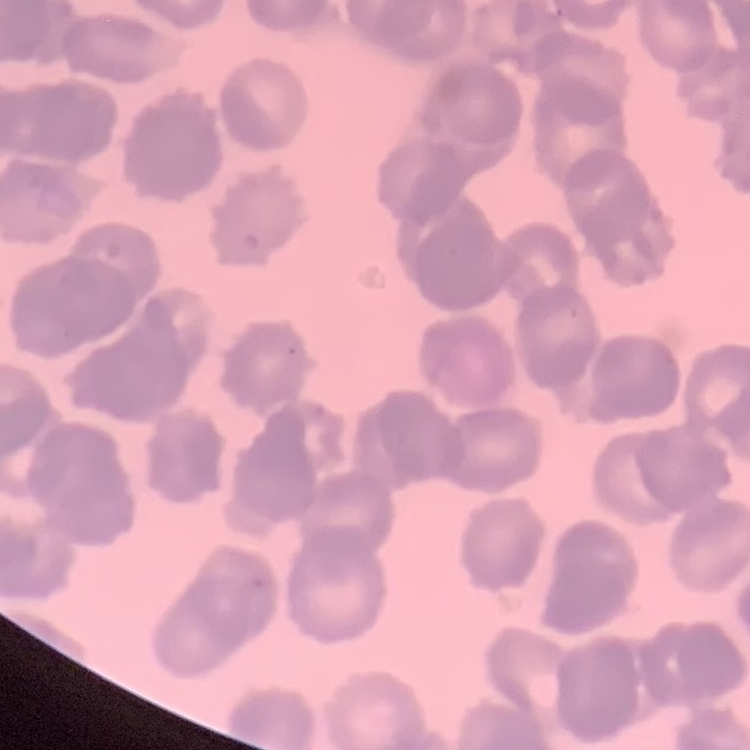 The erythrocytes show rouleaux formation. Thin blood film. Stained with either Field's or Giemsa. Square crop of a larger photomicrograph.